Give the preparation type.
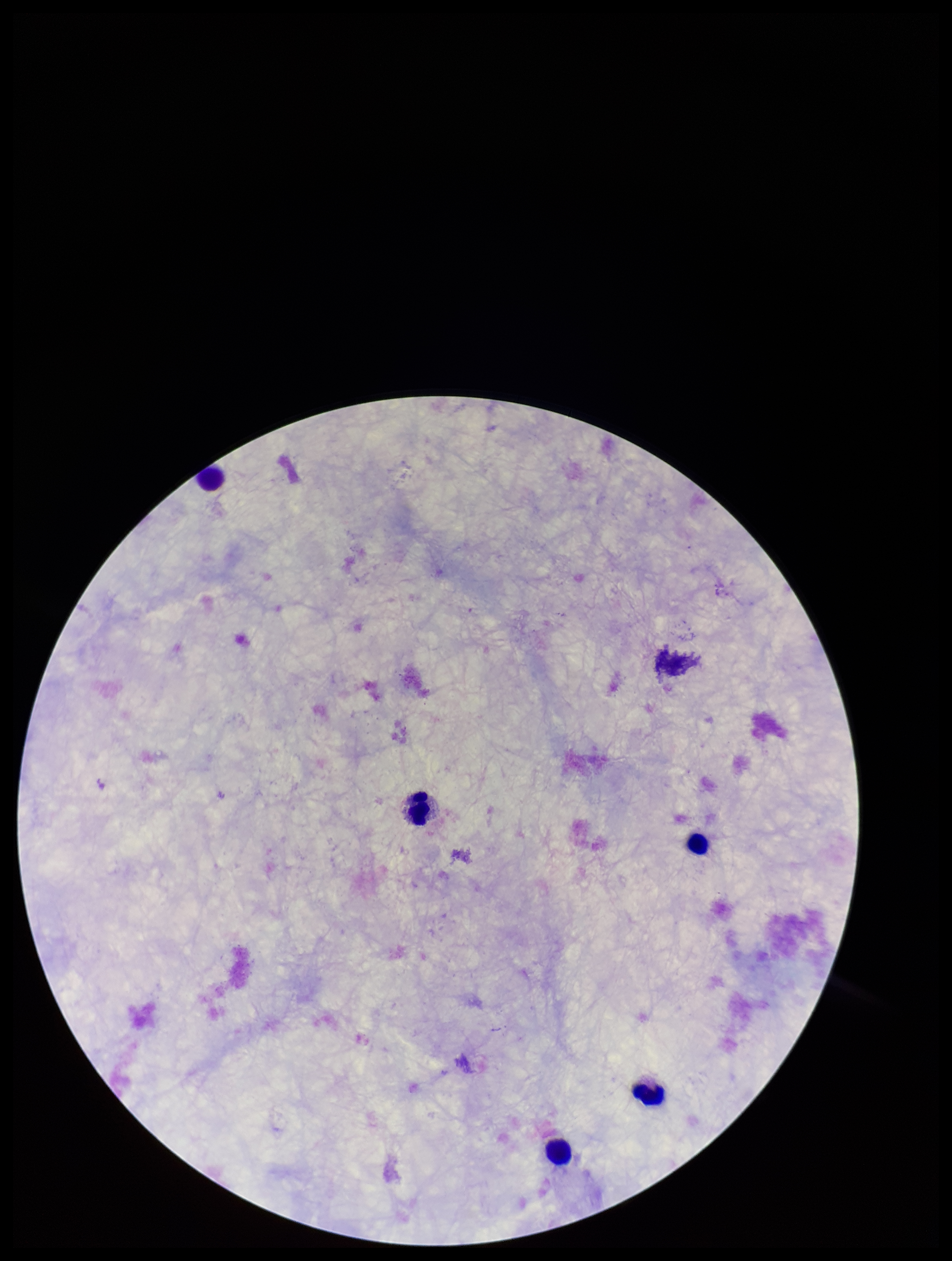

A thick smear.

Image is 952×1261 pixels. Single field of view. Smartphone photograph taken through the eyepiece of a microscope. Plasmodium parasites: none identified. Patient malaria status: negative. Giemsa stain. Parasite count: 0. Leukocyte count: 5.